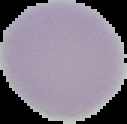
Malaria status: uninfected. Segmented cell region on a black background. Image is 127×124 pixels. From a thin blood smear.